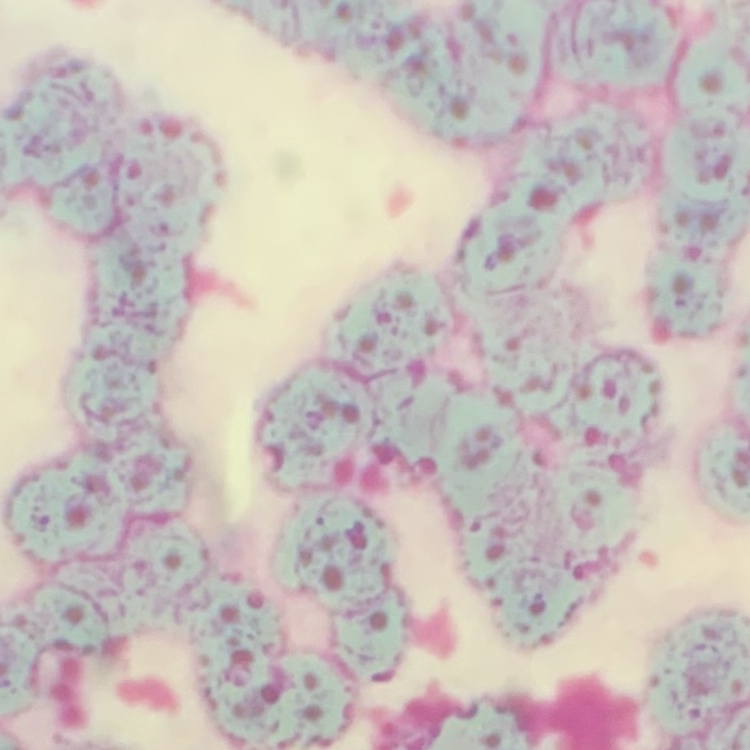
The red blood cells exhibit rouleaux formation. Thin peripheral smear. Stained with either Field's or Giemsa. One tile cut from a larger photomicrograph.